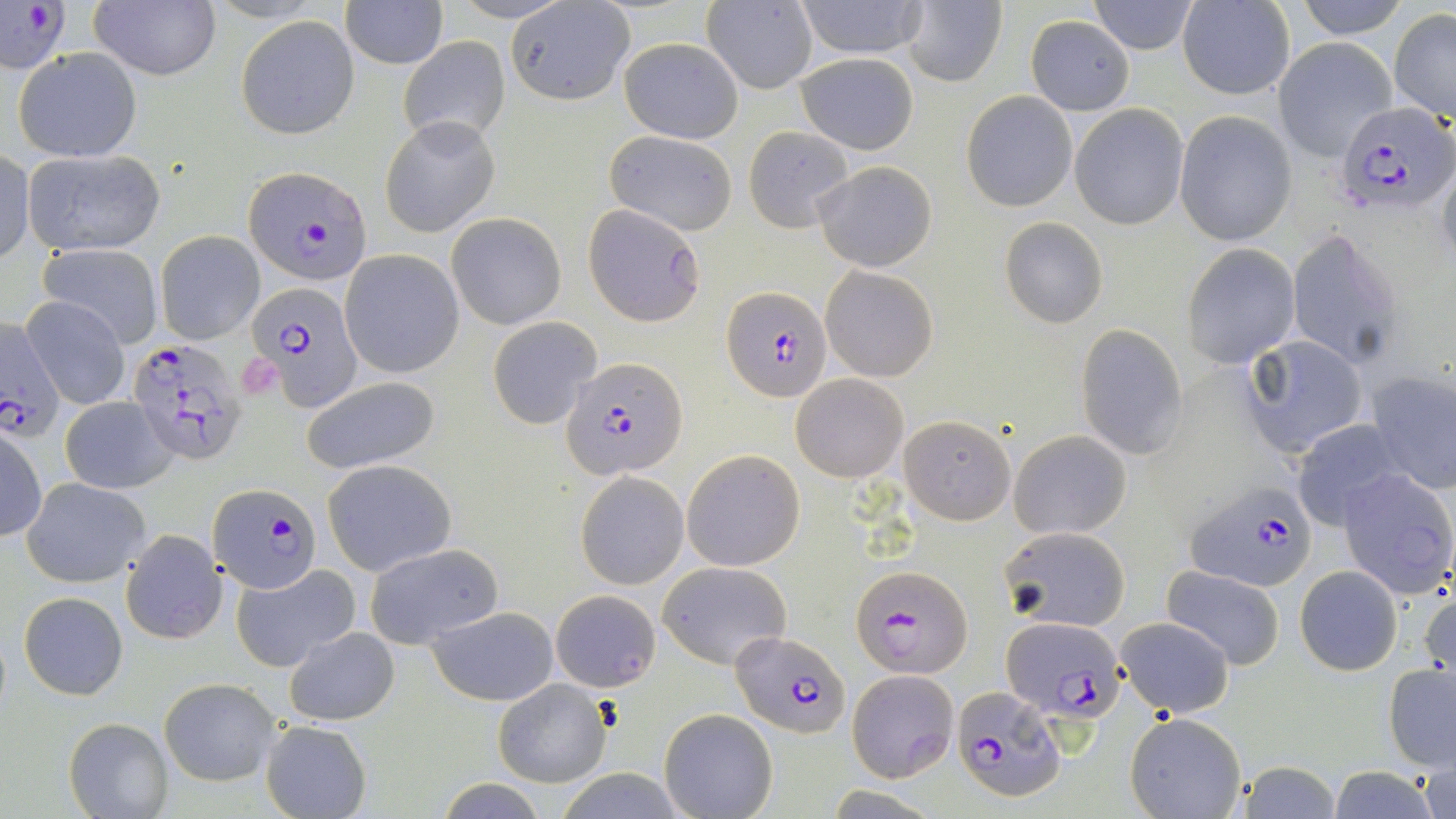
Summary:
  - Coordinate format: approximate bounding boxes as (x1,y1)-(x2,y2) corner pairs in pixels
  - Plasmodium falciparum-infected red blood cell locations: (1332,101)-(1454,220), (243,165)-(371,285), (583,204)-(707,327), (246,281)-(363,410), (723,287)-(831,401), (0,319)-(66,445), (126,335)-(248,464), (565,357)-(688,481), (1185,481)-(1318,591), (209,482)-(320,594), (853,564)-(973,678), (1002,616)-(1128,722), (731,633)-(850,739), (951,686)-(1065,805)
  - Uninfected red blood cell locations: (0,0)-(70,80), (792,0)-(928,59), (901,0)-(1008,88), (1088,0)-(1198,54), (1292,0)-(1413,39), (89,1)-(221,82), (341,1)-(446,69), (1177,1)-(1295,100), (505,2)-(634,105), (702,2)-(817,94), (1389,9)-(1456,122), (237,16)-(359,139), (1024,16)-(1135,115), (398,36)-(511,142), (618,37)-(743,143), (1273,39)-(1395,160), (13,47)-(142,163), (795,53)-(919,155), (961,91)-(1078,211), (1070,103)-(1189,230), (1174,110)-(1297,246), (380,115)-(500,239), (743,126)-(856,232), (603,130)-(738,236), (0,149)-(35,266), (21,149)-(166,256), (1436,157)-(1456,279), (813,161)-(938,273), (446,211)-(569,331), (1000,216)-(1109,329), (154,229)-(264,344), (1285,231)-(1407,372), (37,243)-(164,349), (1181,244)-(1300,369), (339,250)-(464,379), (821,266)-(938,382), (20,297)-(130,412), (488,315)-(602,428), (1075,324)-(1190,459), (1236,336)-(1370,458), (1363,369)-(1455,496), (789,373)-(908,482), (300,376)-(441,475), (60,395)-(178,494), (897,415)-(1016,524), (1290,419)-(1410,531), (0,424)-(46,542), (1008,429)-(1131,539), (681,449)-(805,571), (322,459)-(457,575), (1336,467)-(1456,600), (574,470)-(689,590), (20,477)-(151,587), (999,527)-(1130,631), (119,528)-(227,645), (362,543)-(504,649), (231,562)-(360,673), (657,562)-(791,670), (1296,565)-(1402,676), (1161,566)-(1286,671), (1420,587)-(1455,690), (552,588)-(660,689), (17,591)-(129,700), (425,606)-(560,706), (1115,617)-(1235,716), (284,626)-(400,726), (1383,662)-(1456,774), (846,669)-(958,782), (161,678)-(279,785), (493,679)-(611,786), (659,709)-(779,819), (1124,711)-(1248,818), (64,717)-(175,818), (260,719)-(372,819), (1232,759)-(1345,819), (1422,759)-(1455,819), (1326,767)-(1444,819)
  - Slide-level diagnosis: Plasmodium falciparum
  - Field of view: single
  - Modality: light microscopy
  - Stain: May-Grünwald-Giemsa
  - Preparation: thin blood smear
  - Magnification: 1000x
  - Image size: 1456×819 pixels